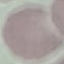

Summary:
  - Malaria status: uninfected
  - Capture: smartphone through the microscope eyepiece
  - Preparation: thin blood film
  - Image type: cell patch, automatically extracted from a larger field of view and resized to 64 × 64 pixels
  - Stain: Giemsa